Identify the blood parasite species.
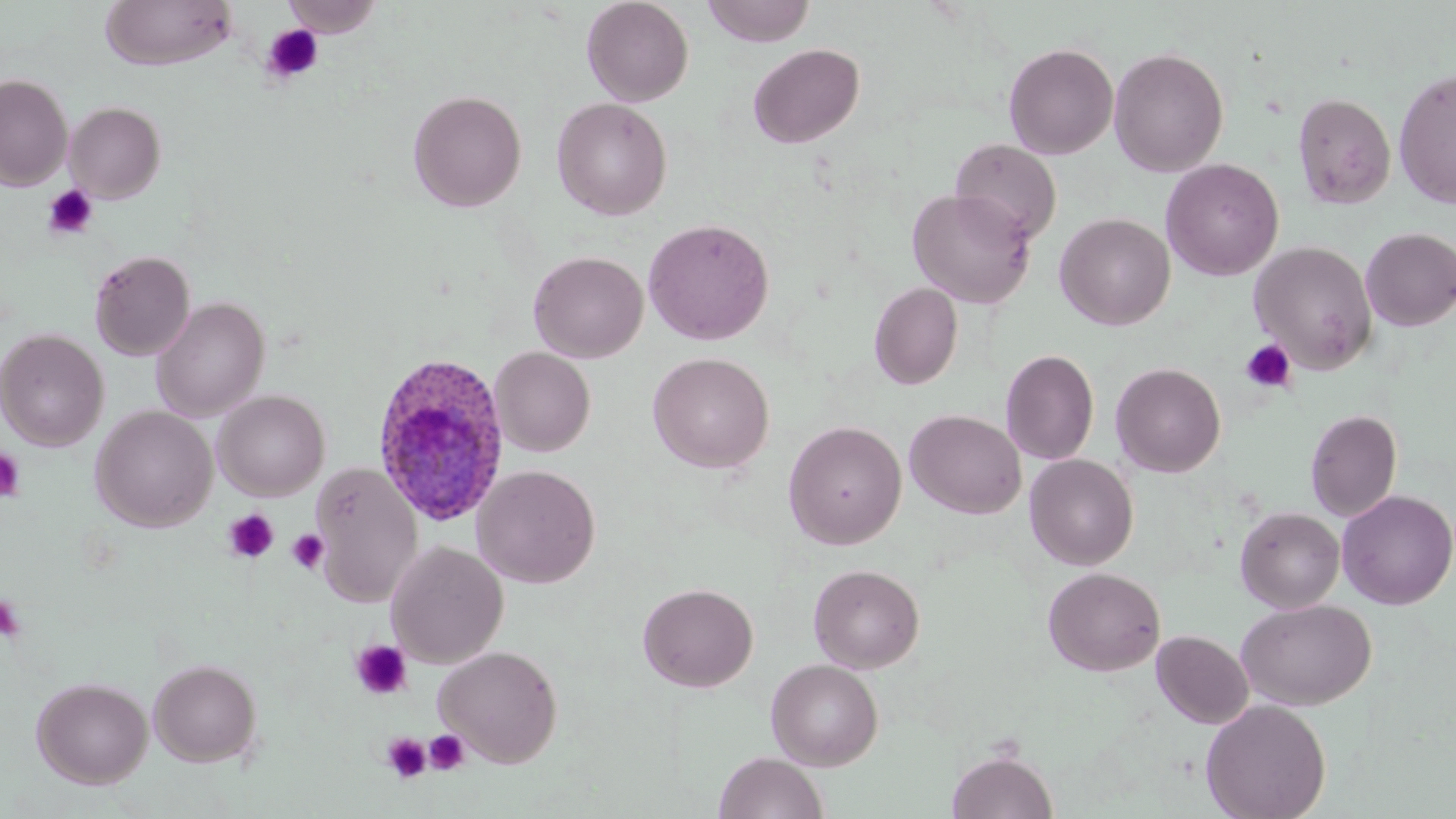

Plasmodium ovale.

{
  "field_of_view": "single",
  "image_size": "1456×819 pixels",
  "preparation": "thin blood smear",
  "plasmodium_ovale_infected_red_blood_cell_locations": "approximate bounding boxes as (x1,y1)-(x2,y2) corner pairs in pixels: (371,352)-(513,528)",
  "stain": "May-Grünwald-Giemsa",
  "magnification": "1000x",
  "platelet_locations": "approximate bounding boxes as (x1,y1)-(x2,y2) corner pairs in pixels: (261,24)-(324,84), (42,184)-(99,240), (1239,338)-(1297,394), (0,448)-(27,503), (223,509)-(280,563), (286,529)-(330,574), (0,593)-(25,643), (350,640)-(413,700), (424,730)-(470,775), (382,732)-(431,784)",
  "modality": "optical microscopy",
  "uninfected_red_blood_cell_locations": "approximate bounding boxes as (x1,y1)-(x2,y2) corner pairs in pixels: (282,0)-(384,38), (582,0)-(694,106), (702,0)-(816,46), (99,1)-(238,71), (1003,42)-(1119,159), (747,43)-(865,148), (1109,46)-(1229,177), (1393,67)-(1456,209), (0,73)-(73,191), (408,90)-(526,211), (1291,92)-(1396,209), (552,97)-(672,220), (65,101)-(166,203), (949,138)-(1062,246), (1161,158)-(1284,281), (907,188)-(1036,308), (1055,213)-(1175,331), (643,218)-(775,345), (1360,227)-(1456,331), (1249,241)-(1377,372), (89,250)-(195,360), (529,250)-(648,363), (869,282)-(963,390), (151,297)-(270,422), (0,329)-(109,452), (490,347)-(595,456), (1000,349)-(1100,465), (647,352)-(774,473), (1111,362)-(1226,477), (213,390)-(330,501), (90,406)-(217,532), (1305,408)-(1403,522), (905,409)-(1026,520), (784,421)-(907,549), (1024,454)-(1138,570), (310,462)-(423,608), (472,465)-(601,589), (1336,489)-(1456,610), (1235,506)-(1345,613), (386,540)-(509,668), (809,564)-(925,673), (1043,567)-(1165,676), (638,582)-(759,692), (1236,599)-(1376,710), (1152,630)-(1253,728), (434,645)-(563,767), (148,658)-(262,767), (766,658)-(884,770), (31,676)-(153,789), (1201,699)-(1331,819), (947,748)-(1059,819), (714,752)-(828,819)"
}